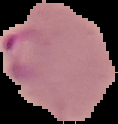

From a thin blood smear. Result: Plasmodium parasites detected. Segmented cell region on a black background. Image is 118×124 pixels.